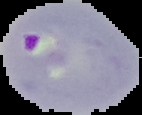

preparation = thin blood smear
image type = cell region segmented out of the field of view; surrounding area masked to black
image size = 142×115 pixels
result = malaria parasites identified